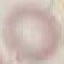

{
  "result": "negative for malaria parasites",
  "image_type": "automatically extracted cell patch, resized to 64 × 64 pixels",
  "capture": "smartphone camera at the microscope eyepiece",
  "preparation": "thin smear",
  "stain": "Giemsa"
}